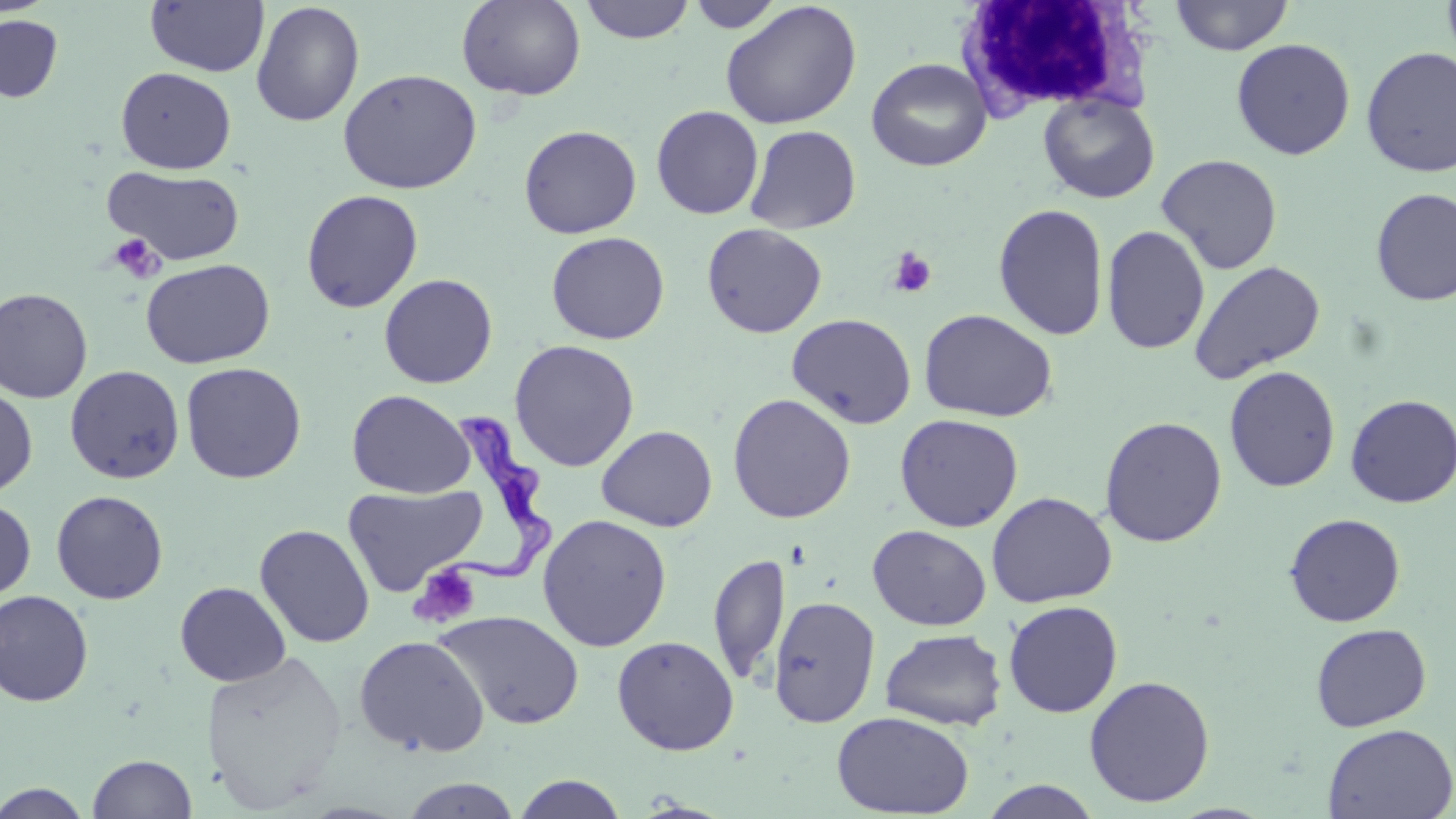
{
  "slide_level_diagnosis": "Trypanosoma brucei",
  "preparation": "thin blood film",
  "magnification": "1000x",
  "image_size": "1456×819 pixels",
  "modality": "light microscopy",
  "white_blood_cell_locations": "approximate bounding boxes as named x1/y1/x2/y2 corners in pixels: (x1=956, y1=2, x2=1154, y2=121)",
  "uninfected_red_blood_cell_locations": "approximate bounding boxes as named x1/y1/x2/y2 corners in pixels: (x1=457, y1=0, x2=586, y2=101), (x1=579, y1=0, x2=695, y2=44), (x1=1169, y1=0, x2=1294, y2=55), (x1=1441, y1=0, x2=1456, y2=68), (x1=145, y1=1, x2=269, y2=78), (x1=687, y1=1, x2=784, y2=32), (x1=720, y1=1, x2=862, y2=130), (x1=251, y1=2, x2=364, y2=127), (x1=0, y1=15, x2=63, y2=102), (x1=1231, y1=38, x2=1356, y2=160), (x1=1360, y1=46, x2=1456, y2=178), (x1=866, y1=57, x2=992, y2=172), (x1=115, y1=66, x2=236, y2=174), (x1=338, y1=68, x2=482, y2=195), (x1=1038, y1=92, x2=1160, y2=204), (x1=651, y1=105, x2=764, y2=219), (x1=518, y1=124, x2=642, y2=239), (x1=744, y1=124, x2=861, y2=234), (x1=1156, y1=153, x2=1282, y2=275), (x1=103, y1=165, x2=245, y2=266), (x1=1371, y1=188, x2=1456, y2=306), (x1=301, y1=189, x2=423, y2=313), (x1=992, y1=203, x2=1110, y2=340), (x1=701, y1=222, x2=827, y2=338), (x1=1101, y1=225, x2=1211, y2=355), (x1=545, y1=231, x2=670, y2=345), (x1=141, y1=258, x2=275, y2=369), (x1=1188, y1=260, x2=1326, y2=384), (x1=378, y1=273, x2=498, y2=389), (x1=0, y1=287, x2=93, y2=403), (x1=918, y1=309, x2=1057, y2=423), (x1=786, y1=312, x2=917, y2=429), (x1=509, y1=339, x2=640, y2=472), (x1=180, y1=361, x2=307, y2=484), (x1=64, y1=365, x2=185, y2=484), (x1=1224, y1=365, x2=1341, y2=492), (x1=0, y1=384, x2=38, y2=498), (x1=347, y1=389, x2=474, y2=499), (x1=727, y1=393, x2=856, y2=523), (x1=1344, y1=393, x2=1456, y2=508), (x1=894, y1=413, x2=1024, y2=532), (x1=1100, y1=415, x2=1227, y2=547), (x1=596, y1=425, x2=718, y2=532), (x1=342, y1=484, x2=488, y2=597), (x1=51, y1=490, x2=169, y2=604), (x1=985, y1=491, x2=1118, y2=608), (x1=0, y1=499, x2=36, y2=604), (x1=537, y1=513, x2=672, y2=652), (x1=1284, y1=513, x2=1406, y2=627), (x1=254, y1=523, x2=375, y2=648), (x1=867, y1=524, x2=991, y2=631), (x1=707, y1=552, x2=789, y2=687), (x1=175, y1=581, x2=291, y2=686), (x1=0, y1=589, x2=94, y2=707), (x1=768, y1=595, x2=880, y2=728), (x1=1003, y1=600, x2=1123, y2=718), (x1=433, y1=609, x2=584, y2=730), (x1=1310, y1=623, x2=1432, y2=732), (x1=880, y1=629, x2=1007, y2=730), (x1=353, y1=635, x2=490, y2=757), (x1=612, y1=635, x2=739, y2=755), (x1=200, y1=648, x2=349, y2=814), (x1=1083, y1=675, x2=1215, y2=807), (x1=832, y1=710, x2=974, y2=818), (x1=1322, y1=723, x2=1456, y2=818), (x1=87, y1=753, x2=198, y2=819), (x1=511, y1=775, x2=628, y2=818), (x1=398, y1=778, x2=523, y2=817), (x1=978, y1=779, x2=1104, y2=819), (x1=1, y1=782, x2=93, y2=818)",
  "platelet_locations": "approximate bounding boxes as named x1/y1/x2/y2 corners in pixels: (x1=107, y1=233, x2=166, y2=282), (x1=887, y1=248, x2=936, y2=298), (x1=408, y1=562, x2=482, y2=629)",
  "stain": "May-Grünwald-Giemsa",
  "field_of_view": "one of a larger specimen",
  "trypanosoma_brucei_locations": "approximate bounding boxes as named x1/y1/x2/y2 corners in pixels: (x1=425, y1=410, x2=559, y2=583)"
}